Assess the morphology of the erythrocytes.
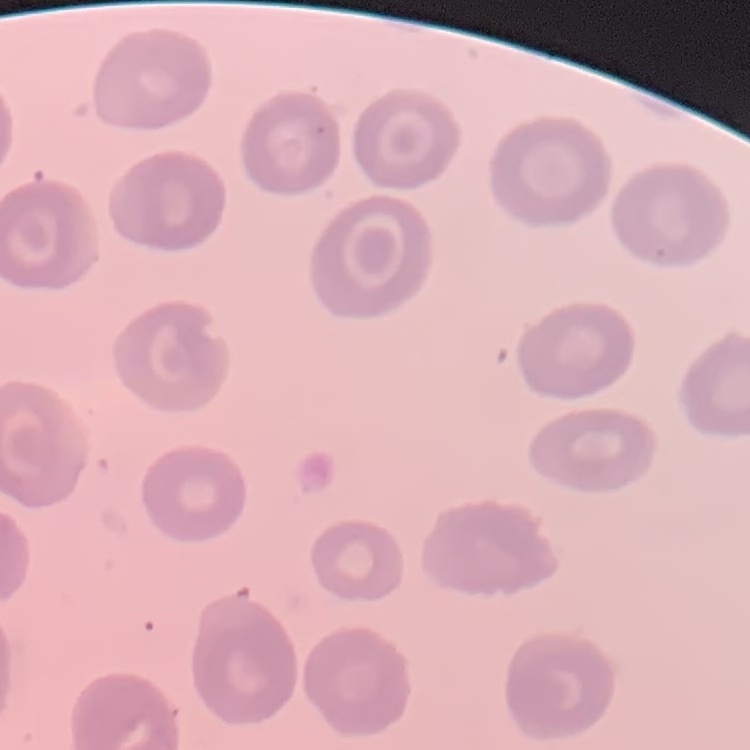
They show no rouleaux formation.

Summary:
  - Stain: Field's or Giemsa
  - Image type: square crop of a larger photomicrograph
  - Preparation: thin blood film